Report the malaria status of this cell.
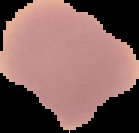

It is uninfected.

Summary:
  - Preparation: thin blood smear
  - Image size: 139×133 pixels
  - Image type: cell region segmented out of the field of view; surrounding area masked to black